Name the blood parasite species.
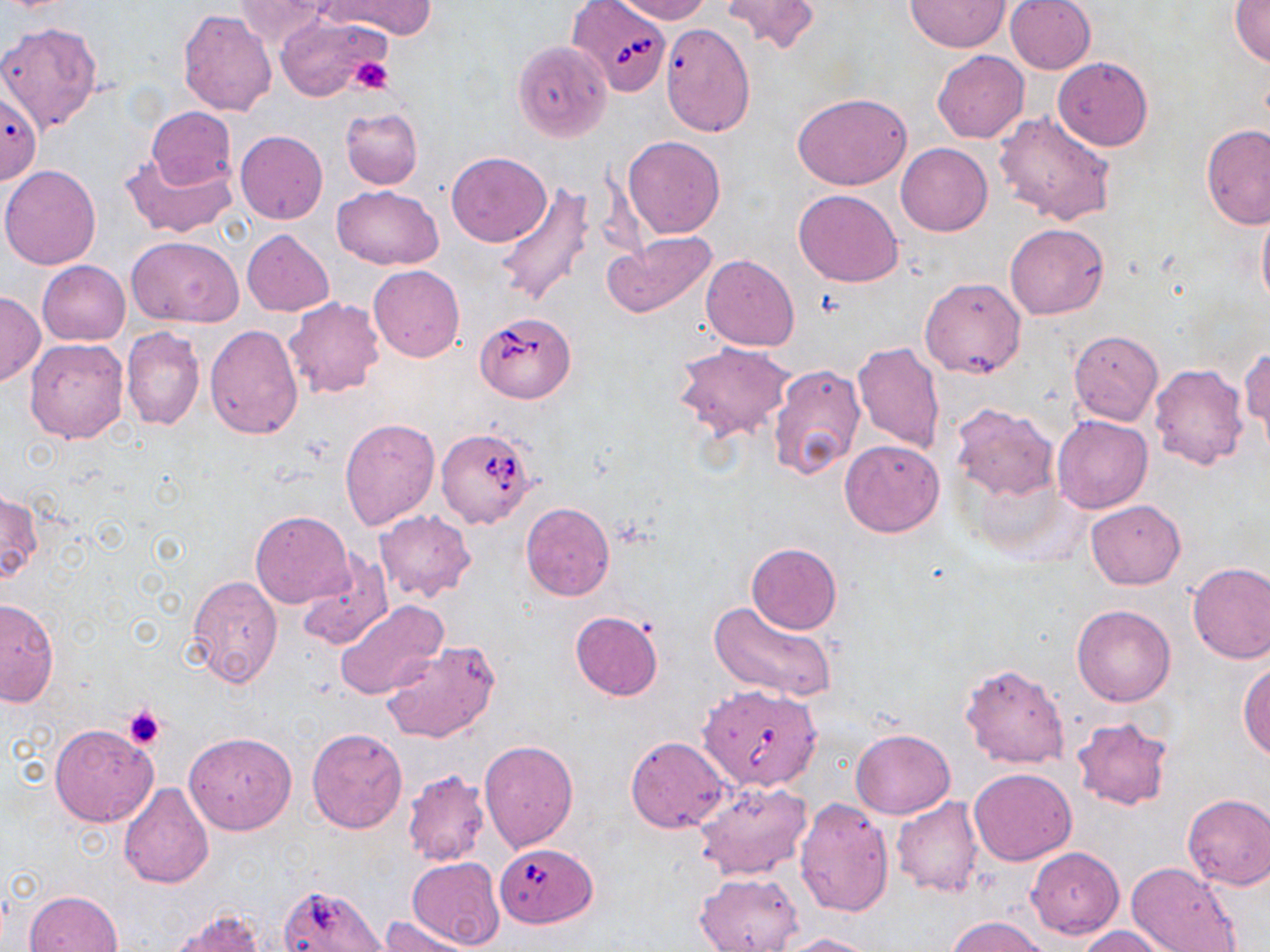

Babesia divergens.

Approximate bounding boxes as [x1, y1, x2, y2] in pixels. Babesia divergens-infected red blood cell locations: [568, 0, 672, 96], [475, 314, 575, 403], [437, 426, 537, 528], [699, 682, 821, 791], [496, 842, 597, 928]. Platelet locations: [348, 57, 394, 94], [123, 705, 166, 750]. Uninfected red blood cell locations: [322, 0, 436, 39], [615, 0, 711, 25], [719, 0, 821, 55], [903, 0, 1011, 51], [1006, 0, 1095, 74], [235, 2, 339, 48], [1231, 2, 1270, 69], [178, 8, 277, 115], [274, 12, 390, 102], [0, 21, 101, 134], [659, 23, 756, 136], [512, 40, 611, 141], [932, 51, 1029, 143], [1053, 56, 1153, 151], [792, 92, 913, 190], [146, 106, 237, 192], [341, 107, 422, 189], [994, 109, 1116, 226], [1201, 124, 1270, 230], [235, 130, 328, 224], [623, 136, 726, 238], [895, 142, 992, 236], [120, 152, 234, 237], [446, 152, 550, 247], [0, 165, 102, 269], [492, 183, 598, 309], [333, 185, 444, 270], [793, 189, 903, 288], [1256, 200, 1270, 316], [1005, 223, 1109, 320], [243, 229, 334, 316], [604, 231, 719, 321], [127, 236, 242, 326], [701, 254, 798, 352], [37, 261, 129, 346], [369, 265, 465, 362], [920, 277, 1025, 379], [0, 292, 43, 386], [283, 297, 385, 399], [204, 325, 302, 439], [121, 326, 205, 432], [1069, 330, 1163, 425], [25, 337, 128, 444], [671, 340, 796, 444], [852, 341, 945, 452], [1241, 346, 1269, 449], [768, 363, 865, 480], [1150, 363, 1249, 471], [949, 401, 1059, 501], [339, 415, 441, 528], [1053, 416, 1153, 514], [840, 439, 945, 537], [1, 489, 41, 585], [1085, 498, 1186, 589], [520, 502, 614, 601], [250, 510, 354, 608], [373, 510, 476, 602], [746, 543, 841, 634], [295, 553, 394, 651], [1186, 562, 1270, 664], [185, 575, 283, 686], [0, 599, 60, 706], [334, 599, 448, 700], [709, 602, 836, 703], [1072, 605, 1175, 707], [570, 610, 664, 700], [381, 641, 501, 745], [1238, 660, 1269, 761], [960, 663, 1069, 769], [1070, 717, 1173, 811], [49, 723, 158, 825], [306, 728, 408, 833], [850, 728, 955, 819], [185, 732, 296, 835], [624, 736, 728, 833], [479, 740, 578, 852], [969, 767, 1077, 865], [402, 769, 491, 866], [694, 781, 812, 880], [118, 784, 215, 888], [1182, 793, 1269, 890], [795, 797, 894, 918], [890, 797, 985, 898], [1026, 846, 1124, 937], [406, 856, 504, 949], [1124, 861, 1242, 952], [695, 871, 804, 951], [25, 889, 124, 952], [168, 908, 265, 952], [380, 915, 477, 952], [948, 915, 1050, 952], [1074, 926, 1169, 952], [776, 933, 885, 952]. Light microscopy. Image is 1270×952 pixels. Captured at 1000x magnification. Single field of view. May-Grünwald-Giemsa-stained preparation. Thin blood film.